Report the malaria status of this cell.
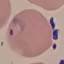
Parasitized.

Summary:
  - Capture: smartphone camera at the microscope eyepiece
  - Image type: cell patch, automatically extracted from a larger field of view and resized to 64 × 64 pixels
  - Preparation: thin blood smear
  - Stain: Giemsa